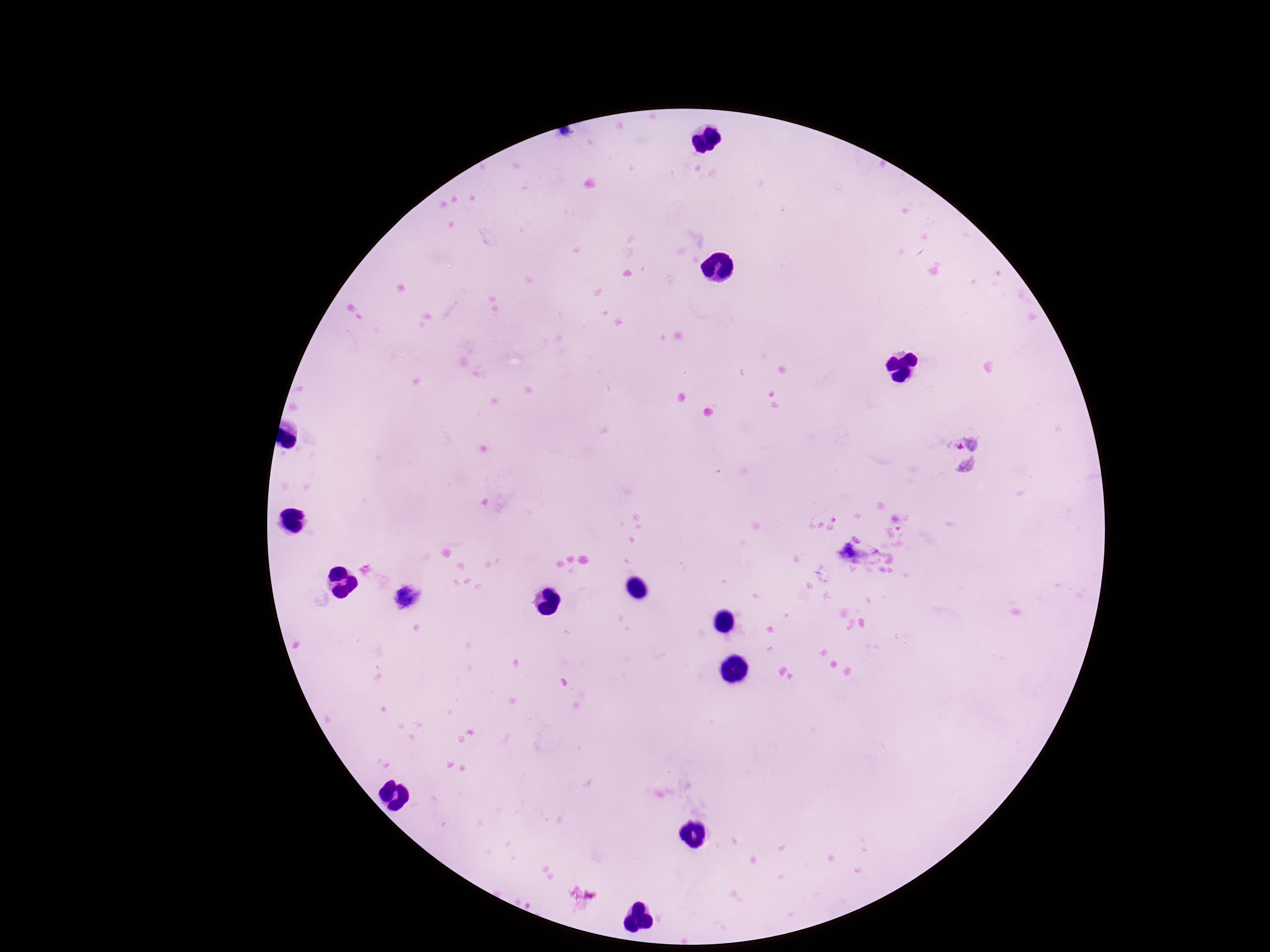 Approximate centers as {x, y} in pixels. Plasmodium parasite locations: {964, 452}, {848, 553}. Thick blood film. Patient malaria status: positive. 100x magnification. Image is 1270×952 pixels. Giemsa-stained preparation. One field from this slide. Smartphone photograph taken through the microscope eyepiece.